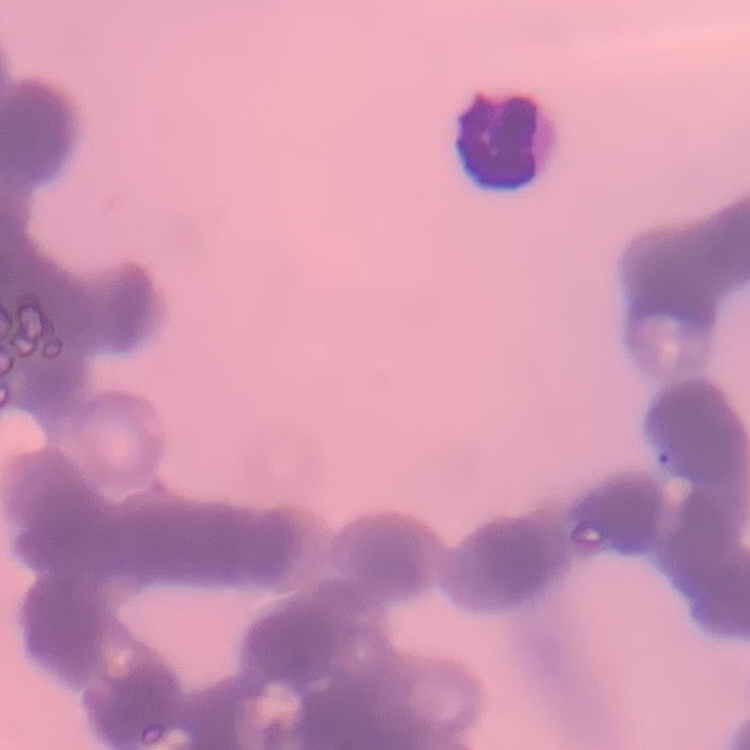
The red blood cells show rouleaux formation. Square crop of a larger photomicrograph. Thin peripheral smear. Stained with either Field's or Giemsa.